Report the malaria status of this cell.
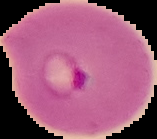

Parasitized.

From a thin blood film. The area outside the segmented cell region is set to black. Image is 157×139 pixels.